Locate every uninfected red blood cell.
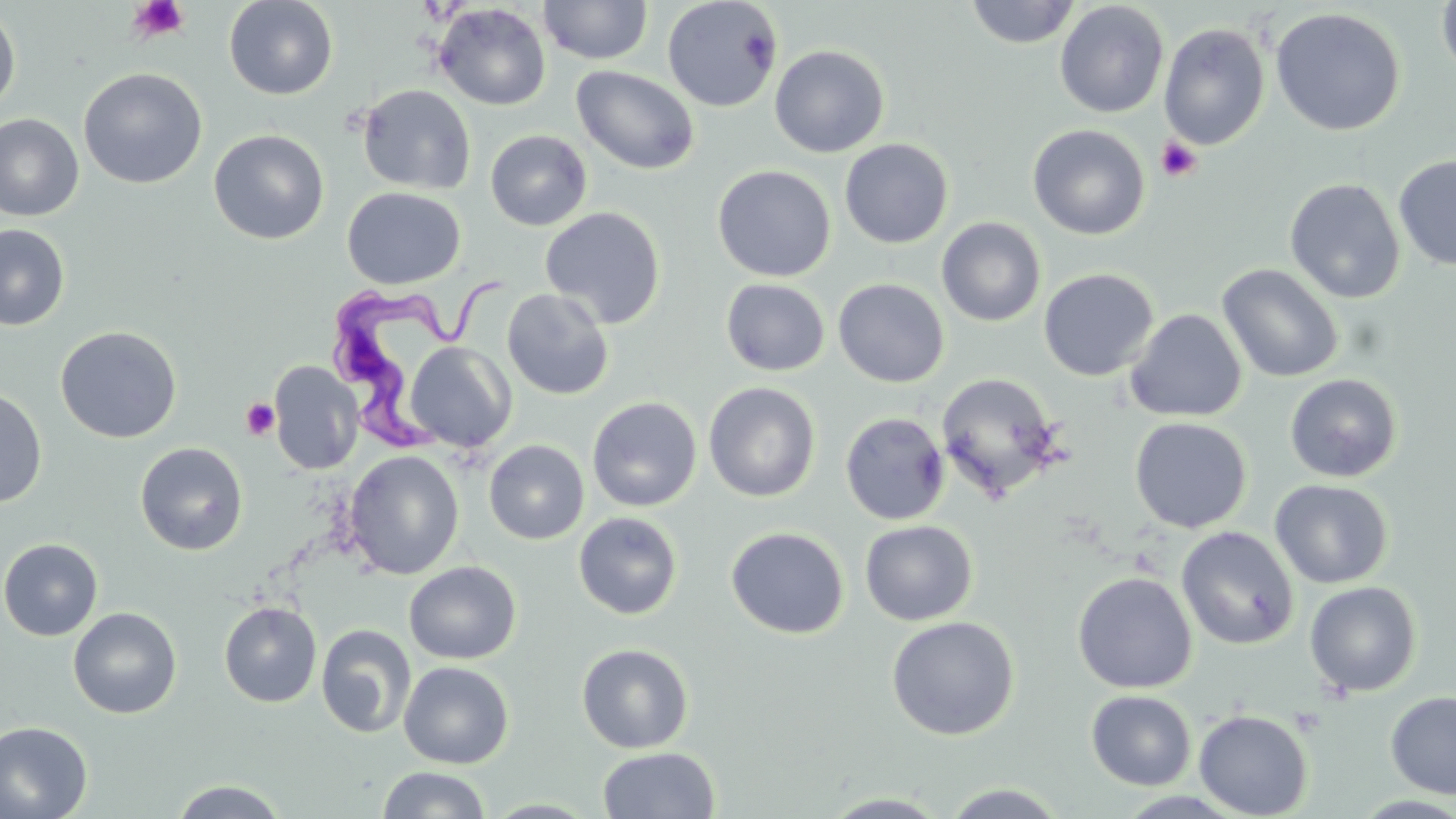
Approximate bounding boxes as (x1, y1, x2, y2) in pixels.
Uninfected red blood cells: (224, 0, 338, 100), (661, 0, 783, 113), (964, 0, 1081, 49), (1436, 0, 1456, 83), (538, 1, 653, 65), (1054, 1, 1170, 118), (433, 3, 551, 111), (0, 5, 21, 116), (1270, 7, 1406, 137), (1158, 22, 1271, 150), (770, 45, 889, 157), (572, 64, 700, 175), (78, 67, 207, 189), (356, 83, 476, 195), (0, 114, 84, 222), (1027, 124, 1150, 240), (208, 129, 329, 244), (485, 129, 592, 231), (839, 138, 954, 249), (1393, 154, 1456, 271), (711, 165, 836, 282), (1285, 178, 1406, 304), (342, 187, 465, 289), (539, 206, 666, 329), (936, 217, 1046, 327), (0, 224, 70, 331), (1216, 263, 1344, 383), (1037, 268, 1160, 382), (720, 278, 831, 376), (833, 278, 950, 388), (501, 288, 615, 400), (1125, 308, 1247, 422), (55, 325, 182, 444), (404, 342, 517, 454), (269, 361, 364, 474), (935, 371, 1066, 502), (1284, 373, 1403, 482), (703, 382, 820, 502), (0, 386, 48, 508), (586, 396, 702, 512), (839, 411, 950, 525), (1129, 416, 1252, 534), (484, 439, 589, 545), (135, 442, 249, 555), (344, 450, 464, 580), (1269, 479, 1393, 588), (573, 511, 683, 619), (860, 520, 977, 626), (726, 526, 849, 638), (1176, 526, 1299, 650), (0, 538, 103, 640), (404, 561, 521, 665), (1072, 571, 1197, 693), (1304, 580, 1422, 697), (219, 601, 322, 708), (68, 606, 182, 719), (886, 615, 1019, 740), (316, 624, 416, 739), (576, 642, 694, 754), (398, 661, 514, 769), (1085, 690, 1196, 791), (1385, 690, 1456, 800), (1085, 695, 1312, 799), (1194, 709, 1313, 818), (0, 721, 94, 819), (597, 747, 720, 818), (376, 766, 492, 818), (169, 779, 288, 818), (938, 783, 1073, 817), (820, 791, 953, 817), (482, 799, 600, 818).

slide-level diagnosis = Trypanosoma brucei
stain = May-Grünwald-Giemsa
modality = optical microscopy
image size = 1456×819 pixels
field of view = single
platelet locations = approximate bounding boxes as (x1, y1, x2, y2) in pixels: (125, 0, 191, 45), (1156, 136, 1202, 183), (240, 398, 280, 440)
magnification = 1000x
Trypanosoma brucei locations = approximate bounding boxes as (x1, y1, x2, y2) in pixels: (328, 275, 519, 462)
preparation = thin blood smear